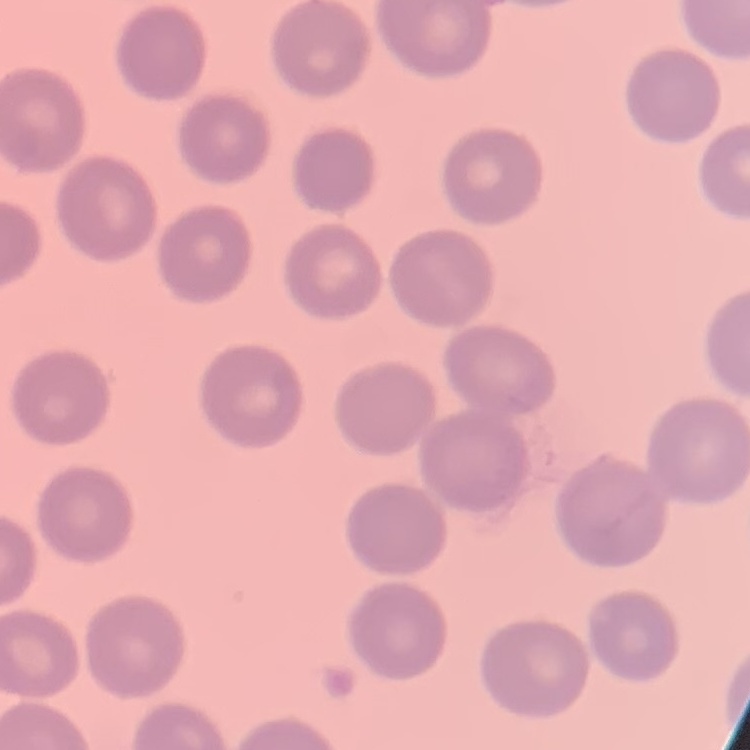
red blood cell morphology = no rouleaux formation
preparation = thin blood film
image type = square crop of a larger photomicrograph
stain = Field's or Giemsa